Assess for parasitized red blood cells.
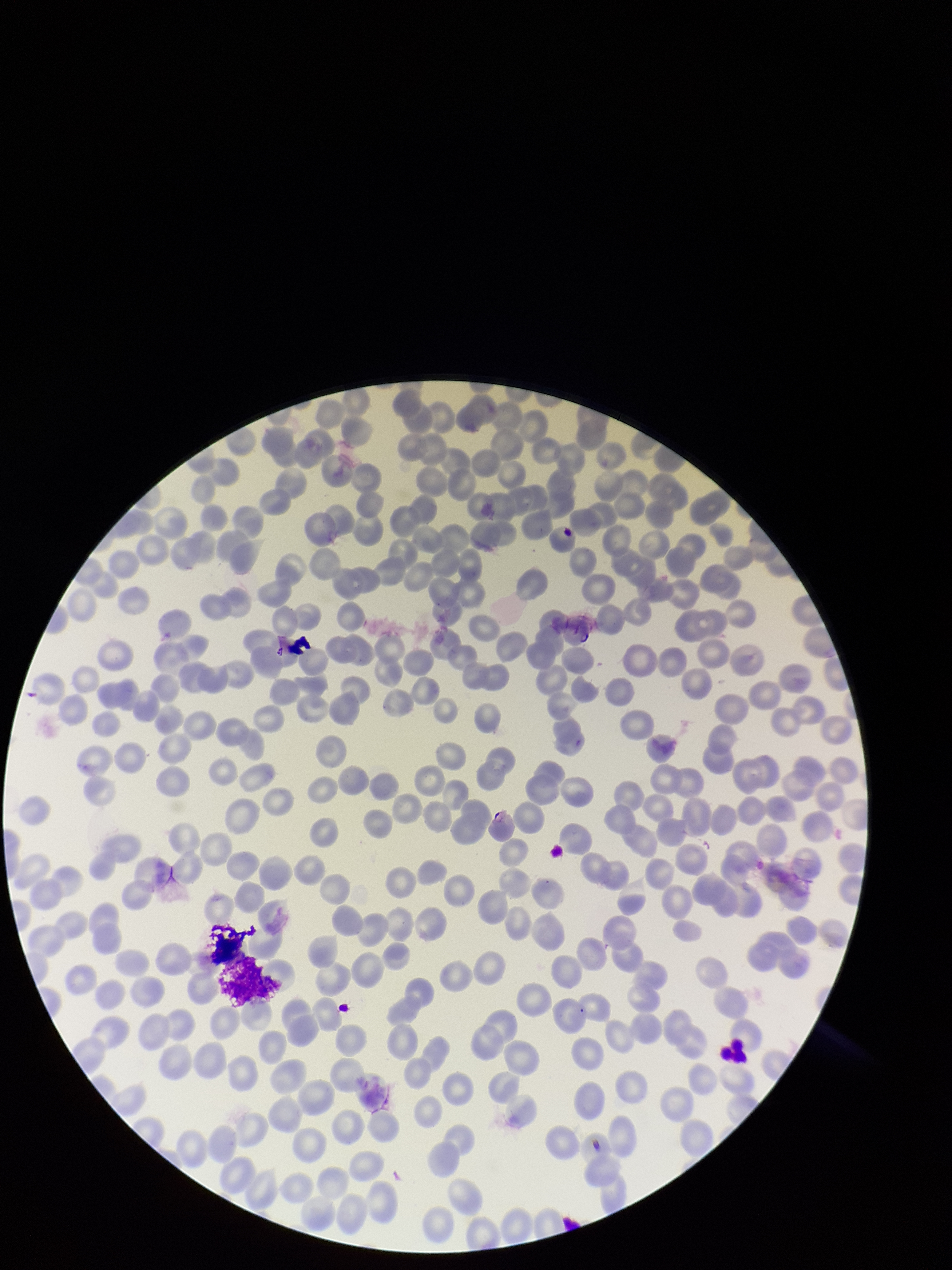
None identified.

Red blood cell count: 243. Patient malaria status: positive. Giemsa stain. Species reported for this patient: Plasmodium falciparum. Photographed through the microscope eyepiece with a smartphone camera. Parasitized red blood cell count: 0. Image is 952×1270 pixels. Preparation: thin. Single field of view.